Draw a bounding box around every Plasmodium parasite.
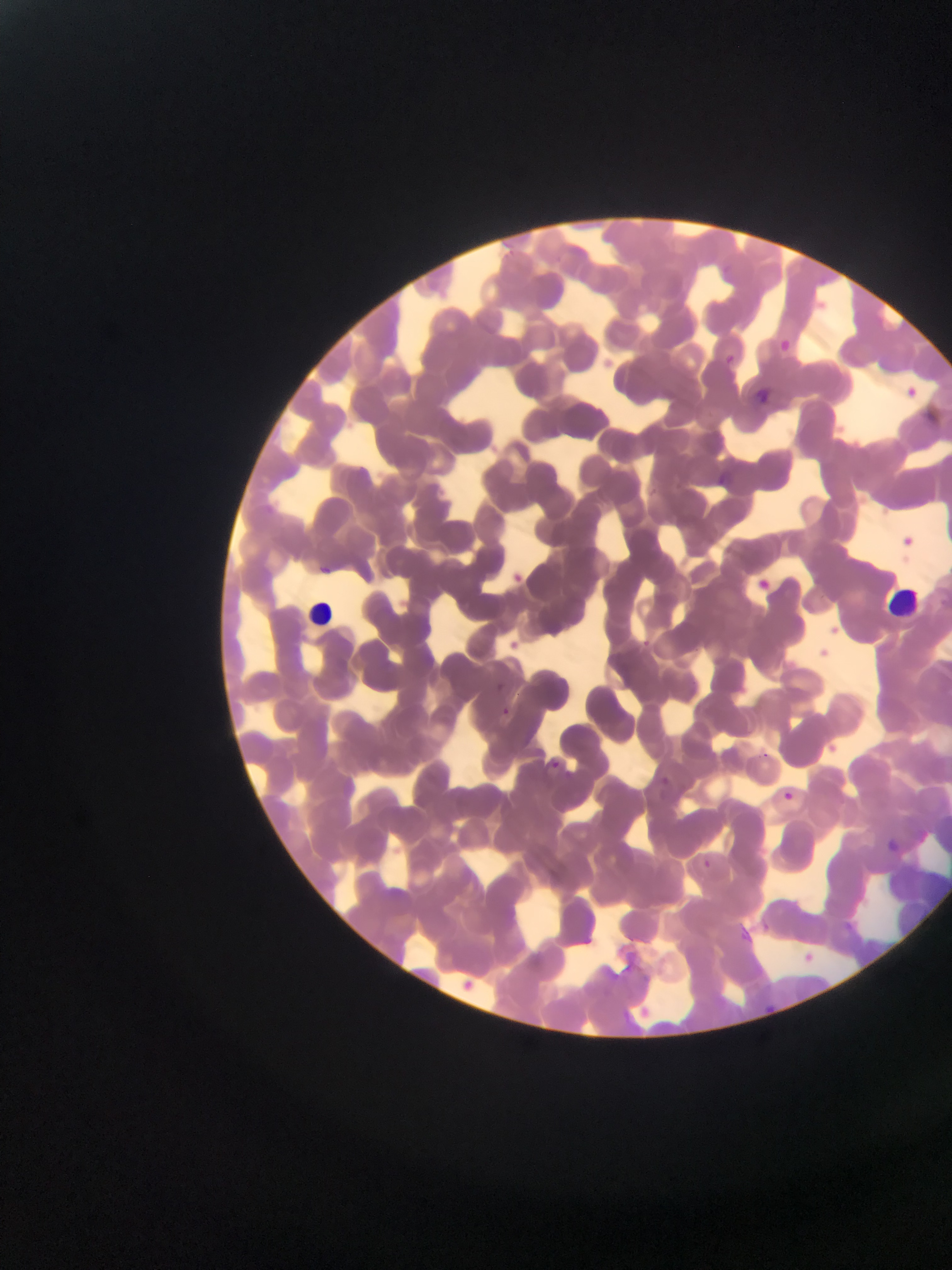

No Plasmodium parasites observed.

image size = 952×1270 pixels
field of view = single
capture = mobile-phone photograph through a microscope
country = Ghana
preparation = thin blood smear
leukocyte locations = approximate bounding boxes as (left, top, right, bottom) in pixels: (890, 581, 928, 616), (301, 593, 337, 630)